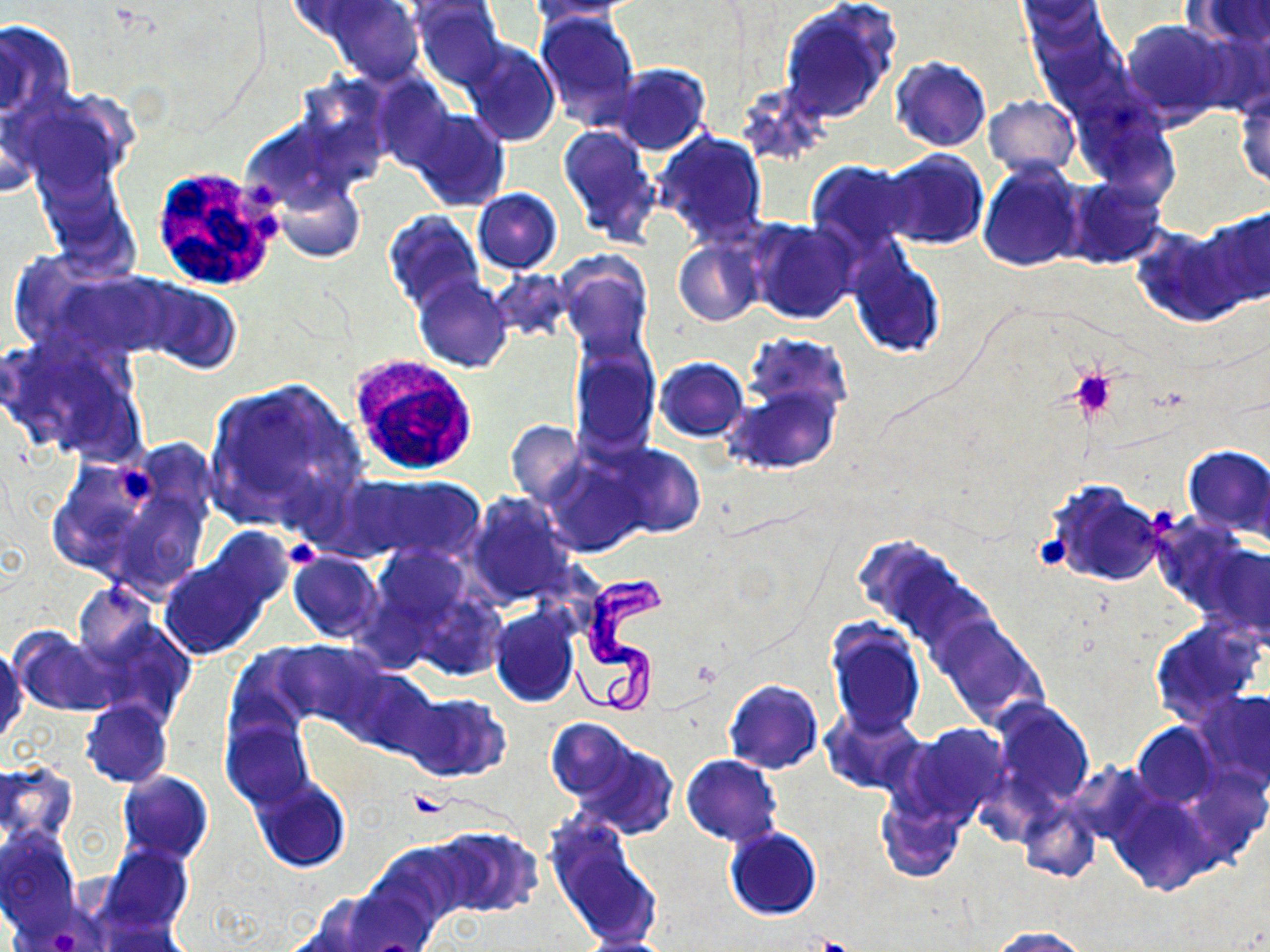
Summary:
  - Coordinate format: approximate bounding boxes as [x1, y1, x2, y2] in pixels
  - White blood cell locations: [148, 163, 283, 292], [345, 353, 481, 478]
  - Platelet locations: [1064, 367, 1119, 421], [115, 469, 158, 502], [1033, 533, 1072, 570], [283, 538, 321, 569], [404, 791, 454, 820], [809, 938, 860, 952]
  - Trypanosoma brucei locations: [572, 574, 672, 722]
  - Uninfected red blood cell locations: [284, 0, 390, 39], [325, 0, 422, 84], [521, 0, 645, 23], [778, 0, 901, 125], [1187, 0, 1270, 44], [410, 2, 505, 84], [535, 10, 639, 130], [1119, 18, 1235, 124], [0, 19, 76, 121], [461, 39, 559, 146], [889, 56, 993, 152], [611, 62, 710, 155], [373, 77, 455, 170], [1234, 87, 1270, 192], [8, 92, 129, 196], [983, 95, 1079, 177], [408, 108, 510, 211], [557, 123, 662, 248], [653, 131, 768, 246], [876, 148, 988, 250], [978, 159, 1088, 271], [806, 160, 917, 257], [36, 168, 139, 275], [274, 178, 367, 263], [1062, 179, 1167, 268], [472, 188, 562, 274], [1198, 206, 1270, 312], [384, 210, 485, 312], [747, 218, 860, 325], [1131, 225, 1250, 325], [674, 238, 763, 326], [848, 251, 945, 358], [558, 253, 653, 358], [36, 269, 172, 363], [413, 274, 513, 372], [130, 277, 243, 372], [1, 333, 144, 461], [744, 334, 853, 419], [569, 344, 658, 456], [655, 357, 748, 441], [203, 377, 367, 527], [729, 384, 841, 473], [505, 419, 585, 509], [606, 443, 706, 539], [1183, 446, 1270, 538], [543, 457, 643, 555], [48, 458, 195, 593], [343, 472, 486, 564], [1044, 478, 1168, 588], [466, 492, 573, 604], [1147, 514, 1252, 615], [160, 542, 285, 657], [365, 543, 482, 654], [1198, 543, 1270, 643], [287, 552, 384, 643], [72, 582, 160, 669], [407, 589, 508, 680], [489, 606, 579, 708], [933, 615, 1046, 728], [85, 616, 198, 728], [826, 619, 925, 737], [1150, 622, 1259, 722], [9, 627, 121, 717], [275, 639, 382, 729], [0, 642, 25, 746], [225, 648, 317, 745], [337, 666, 439, 757], [722, 679, 823, 773], [1197, 688, 1270, 790], [398, 692, 509, 782], [990, 699, 1095, 810], [80, 700, 172, 788], [823, 708, 925, 795], [221, 712, 314, 809], [546, 719, 636, 802], [903, 723, 1011, 821], [1132, 723, 1218, 807], [572, 738, 678, 839], [681, 754, 782, 845], [0, 761, 76, 846], [117, 771, 213, 865], [250, 776, 351, 872], [1110, 794, 1218, 895], [875, 797, 965, 883], [1019, 805, 1100, 883], [546, 818, 659, 947], [430, 826, 541, 919], [0, 828, 80, 936], [724, 828, 821, 920], [369, 841, 473, 929], [102, 844, 193, 936], [338, 876, 442, 952], [989, 926, 1089, 951], [577, 934, 676, 952]
  - Slide-level diagnosis: Trypanosoma brucei
  - Field of view: single
  - Preparation: thin blood smear
  - Modality: light microscopy
  - Magnification: 1000x
  - Stain: May-Grünwald-Giemsa
  - Image size: 1270×952 pixels